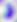

modality = photomicrograph
identification = Toxoplasma gondii
magnification = 400x